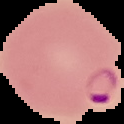

{
  "image_type": "segmented cell region with the area outside set to black",
  "preparation": "thin blood smear",
  "image_size": "124×124 pixels",
  "malaria_status": "parasitized"
}